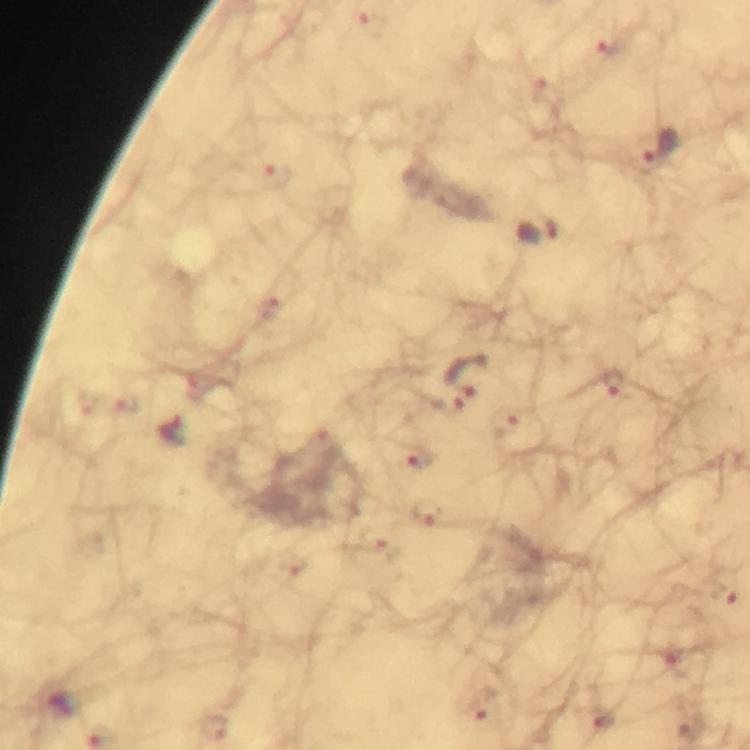 Approximate object centers, in pixels from the top-left corner. Malaria parasite locations: (x=612, y=48), (x=543, y=93), (x=659, y=146), (x=277, y=178), (x=537, y=232), (x=269, y=308), (x=471, y=376), (x=604, y=382), (x=442, y=402), (x=506, y=426), (x=175, y=432), (x=419, y=457), (x=427, y=513), (x=381, y=541), (x=292, y=564), (x=725, y=593), (x=483, y=703), (x=602, y=718), (x=214, y=728). Giemsa stain. Image is 750×750 pixels. Immersion oil was used. 100x magnification. Cropped region of a single field of view. Thick blood smear. Smartphone photograph taken through a microscope. From a malaria diagnostic workup.